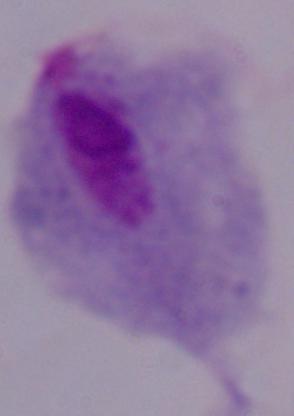
Summary:
  - Magnification: 1000x
  - Modality: micrograph
  - Identification: trichomonad